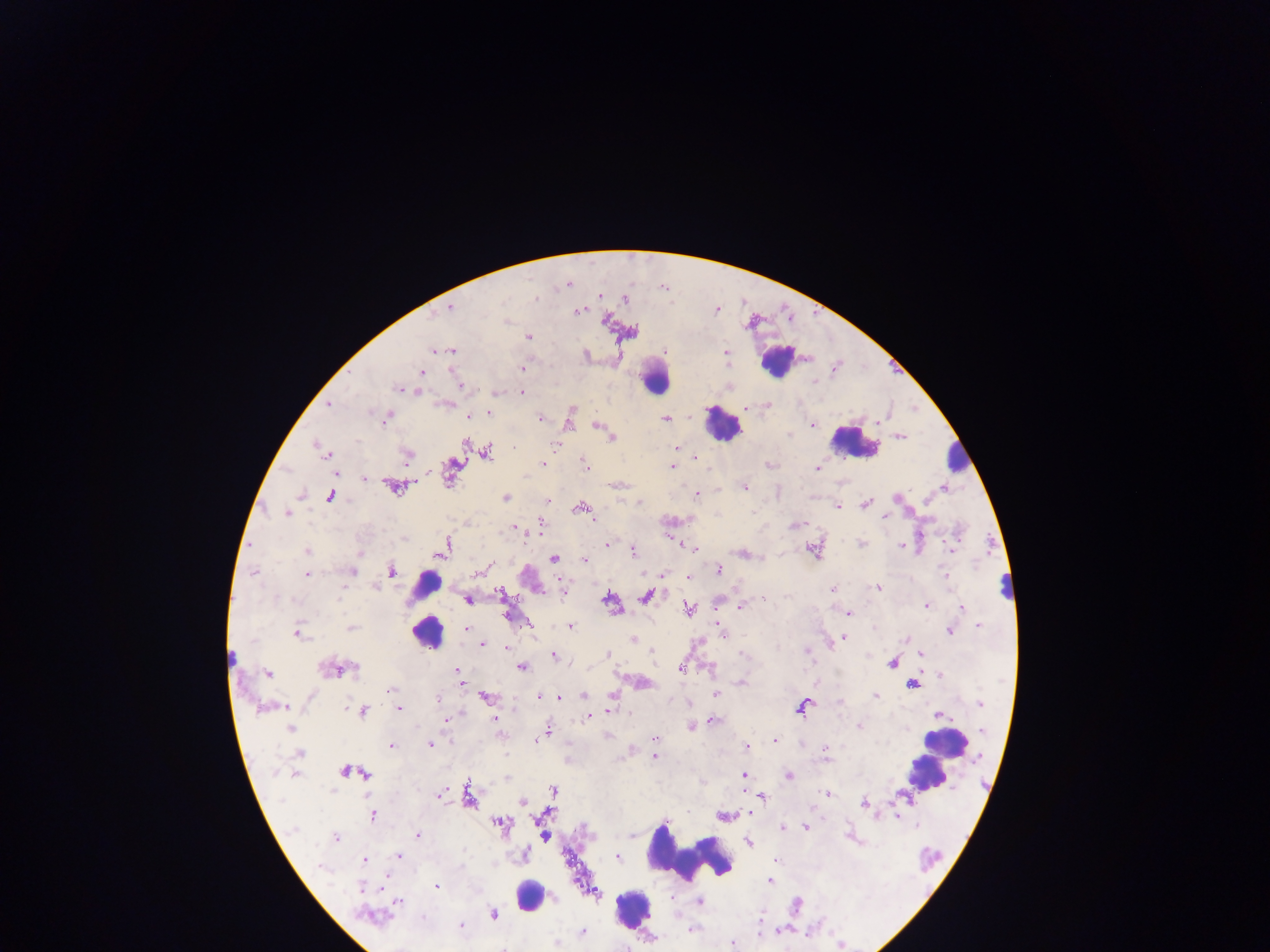
{
  "country": "Ghana",
  "capture": "mobile-phone photograph through a microscope",
  "field_of_view": "single",
  "image_size": "1270×952 pixels",
  "preparation": "thick blood film",
  "plasmodium_parasite_locations": "approximate centers as x y in pixels: 567 284; 599 296; 624 300; 450 307; 577 310; 528 336; 442 350; 451 350; 725 353; 521 368; 421 372; 460 385; 728 385; 400 389; 416 390; 495 392; 521 393; 330 404; 444 404; 767 404; 489 412; 469 416; 386 418; 540 418; 666 419; 568 420; 811 423; 598 425; 900 435; 611 437; 465 441; 318 446; 677 448; 323 450; 485 452; 327 453; 406 456; 695 457; 542 464; 769 464; 586 466; 672 467; 452 468; 817 468; 335 475; 364 478; 618 485; 394 486; 744 487; 943 487; 330 495; 696 495; 898 497; 506 498; 547 501; 638 502; 865 503; 837 506; 580 508; 287 513; 885 516; 541 522; 796 525; 514 527; 674 540; 607 544; 861 544; 900 545; 441 548; 951 548; 694 549; 812 549; 306 551; 633 551; 743 553; 554 558; 584 559; 487 566; 482 569; 390 570; 718 570; 352 571; 253 572; 661 574; 306 575; 688 576; 946 576; 877 587; 832 589; 563 590; 500 593; 647 595; 764 598; 467 600; 609 601; 717 602; 925 605; 742 606; 687 608; 962 609; 847 614; 507 616; 527 623; 720 624; 978 625; 569 626; 350 627; 466 629; 949 631; 297 632; 845 633; 722 634; 845 638; 907 638; 634 640; 481 644; 506 648; 608 653; 742 653; 920 654; 552 656; 892 661; 521 666; 335 669; 680 669; 456 670; 268 674; 939 675; 463 682; 740 682; 911 683; 390 690; 875 694; 612 695; 716 695; 537 696; 583 696; 486 697; 559 697; 439 700; 838 701; 980 703; 686 704; 802 705; 274 706; 284 706; 398 708; 609 710; 362 712; 939 714; 588 717; 495 719; 713 719; 444 720; 858 724; 692 726; 290 728; 547 733; 539 738; 655 738; 534 739; 774 740; 430 744; 391 746; 746 748; 825 752; 299 753; 653 756; 349 771; 295 773; 743 774; 788 776; 553 791; 828 793; 439 794; 762 796; 468 797; 522 802; 863 803; 749 812; 372 815; 725 815; 896 815; 500 824; 806 826; 917 826; 782 828; 417 834; 544 836; 335 838; 748 842; 399 855; 524 855; 616 856; 363 860; 774 860; 321 866; 769 880; 436 887; 362 888; 397 900; 698 901; 493 915; 371 917; 461 925; 690 929; 758 931; 582 933; 556 943; 732 944; 503 947",
  "leukocyte_locations": "approximate centers as x y in pixels: 777 360; 654 376; 723 424; 853 442; 959 457; 425 585; 1005 589; 426 631; 945 743; 936 753; 927 773; 691 853; 531 896; 630 908"
}